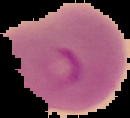
preparation = thin blood smear
image size = 130×118 pixels
malaria status = parasitized
image type = segmented cell region with the area outside set to black